Point out leukocytes.
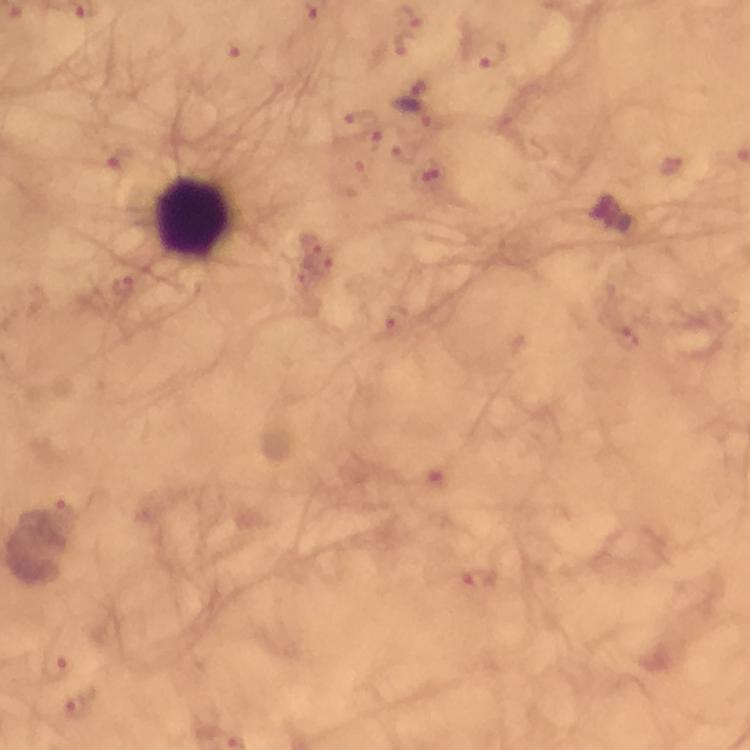

Approximate centers as [x, y] in pixels.
Leukocytes: [191, 218].

Summary:
  - Malaria parasite locations: [403, 45], [240, 50], [491, 60], [408, 98], [356, 118], [369, 138], [399, 153], [113, 159], [670, 166], [433, 175], [348, 179], [311, 239], [316, 267], [124, 286], [395, 318], [627, 338], [479, 579], [55, 667], [77, 705]
  - Capture: smartphone mounted on the microscope
  - Magnification: 100x
  - Stain: Giemsa
  - Immersion oil: used
  - Preparation: thick blood film
  - Cropped from: a single field of view
  - Context: from a malaria diagnostic workup
  - Image size: 750×750 pixels